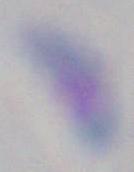

Summary:
  - Magnification: 1000x
  - Modality: micrograph
  - Identification: Toxoplasma gondii